Assess this cell for malaria.
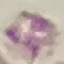
It is uninfected.

image type = automatically extracted cell patch, resized to 64 × 64 pixels
stain = Giemsa
preparation = thin blood film
capture = smartphone camera at the microscope eyepiece